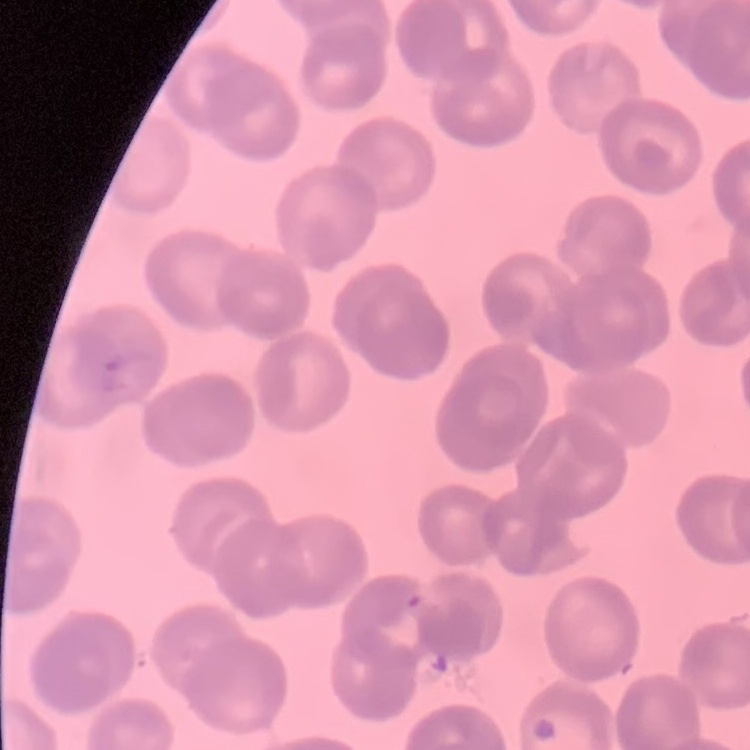

Summary:
  - Erythrocyte morphology: rouleaux formation
  - Image type: one tile cut from a larger photomicrograph
  - Stain: Field's or Giemsa
  - Preparation: thin peripheral smear